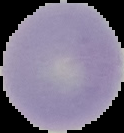
result = no malaria parasites detected
image size = 124×133 pixels
preparation = thin blood smear
image type = segmented cell region on a black background